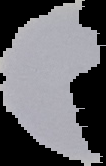
Segmented cell region on a black background. From a thin blood film. Image is 106×166 pixels. Result: malaria parasites identified.